Classify this cell by malaria status.
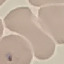
It is uninfected.

Summary:
  - Stain: Giemsa
  - Preparation: thin blood smear
  - Capture: smartphone camera at the microscope eyepiece
  - Image type: cell patch, automatically extracted from a larger field of view and resized to 64 × 64 pixels